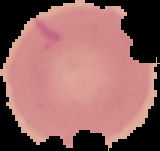

Summary:
  - Image size: 160×151 pixels
  - Malaria status: uninfected
  - Image type: segmented cell region on a black background
  - Preparation: thin blood film